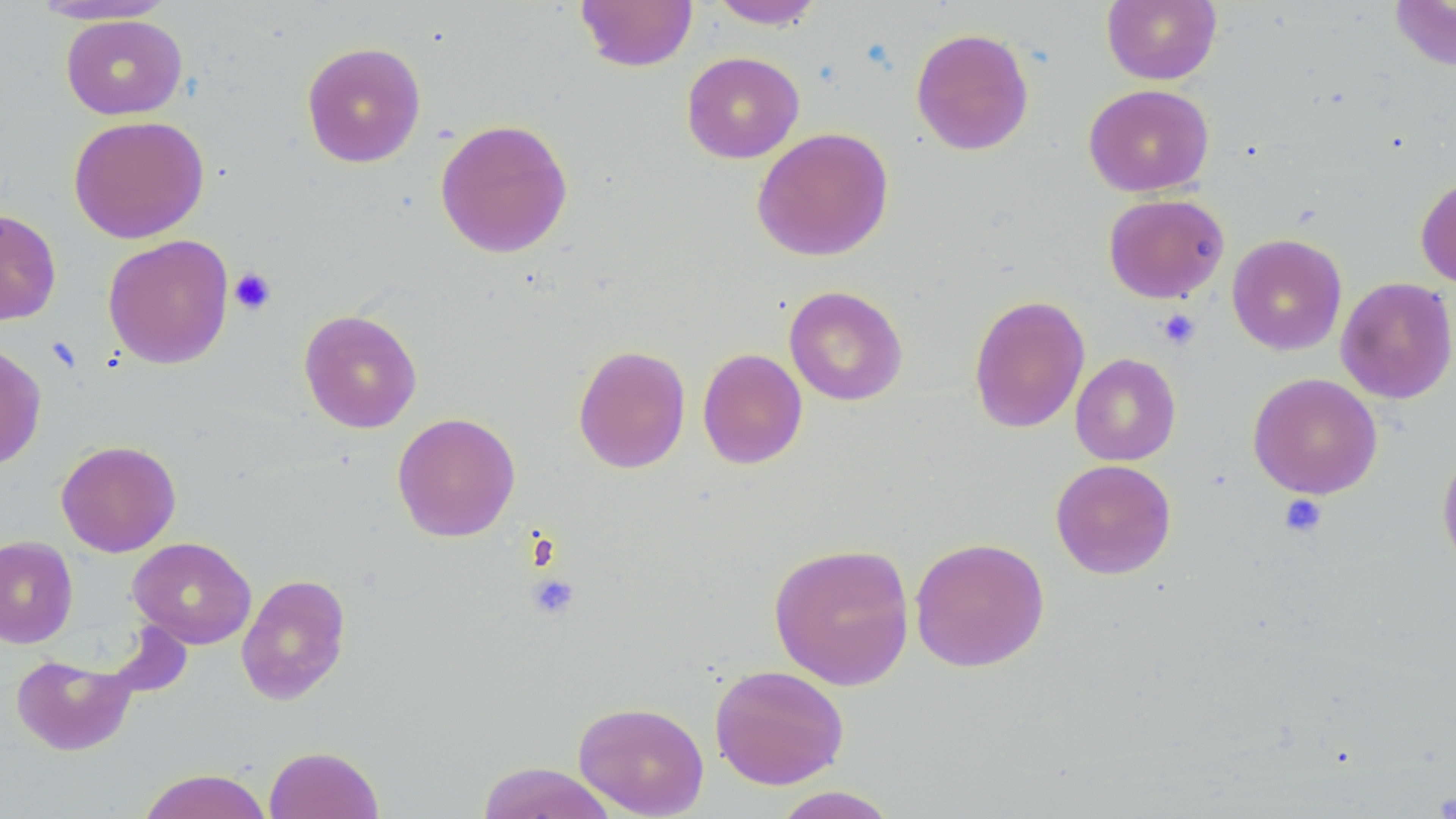

Summary:
  - Coordinate format: approximate bounding boxes as named x1/y1/x2/y2 corners in pixels
  - Platelet locations: (x1=229, y1=267, x2=276, y2=315), (x1=1157, y1=309, x2=1200, y2=350), (x1=1279, y1=494, x2=1327, y2=537), (x1=527, y1=574, x2=580, y2=619), (x1=1434, y1=790, x2=1456, y2=818)
  - Uninfected red blood cell locations: (x1=575, y1=0, x2=697, y2=72), (x1=707, y1=0, x2=827, y2=29), (x1=1102, y1=0, x2=1221, y2=85), (x1=1388, y1=0, x2=1456, y2=72), (x1=28, y1=1, x2=179, y2=26), (x1=60, y1=14, x2=188, y2=120), (x1=911, y1=27, x2=1035, y2=156), (x1=301, y1=41, x2=426, y2=168), (x1=681, y1=51, x2=804, y2=163), (x1=1083, y1=84, x2=1214, y2=197), (x1=68, y1=115, x2=209, y2=244), (x1=435, y1=118, x2=573, y2=258), (x1=751, y1=127, x2=895, y2=262), (x1=1415, y1=175, x2=1456, y2=289), (x1=1103, y1=193, x2=1229, y2=304), (x1=0, y1=208, x2=61, y2=325), (x1=1226, y1=233, x2=1347, y2=355), (x1=102, y1=234, x2=234, y2=369), (x1=1335, y1=277, x2=1456, y2=404), (x1=784, y1=286, x2=908, y2=406), (x1=968, y1=294, x2=1090, y2=434), (x1=299, y1=309, x2=422, y2=433), (x1=0, y1=342, x2=47, y2=470), (x1=572, y1=344, x2=691, y2=474), (x1=697, y1=348, x2=808, y2=469), (x1=1070, y1=353, x2=1181, y2=466), (x1=1247, y1=373, x2=1383, y2=499), (x1=392, y1=412, x2=520, y2=542), (x1=56, y1=440, x2=181, y2=557), (x1=1436, y1=445, x2=1456, y2=574), (x1=1050, y1=459, x2=1177, y2=579), (x1=0, y1=535, x2=78, y2=648), (x1=910, y1=536, x2=1050, y2=672), (x1=128, y1=537, x2=257, y2=649), (x1=767, y1=541, x2=916, y2=690), (x1=236, y1=573, x2=351, y2=705), (x1=11, y1=653, x2=136, y2=756), (x1=709, y1=664, x2=850, y2=789), (x1=573, y1=701, x2=710, y2=817), (x1=264, y1=745, x2=384, y2=819), (x1=475, y1=762, x2=618, y2=819), (x1=137, y1=768, x2=273, y2=819), (x1=770, y1=786, x2=902, y2=818)
  - Slide-level diagnosis: negative for blood parasites
  - Preparation: thin blood film
  - Magnification: 1000x
  - Stain: May-Grünwald-Giemsa
  - Image size: 1456×819 pixels
  - Modality: light microscopy
  - Field of view: one of a larger specimen